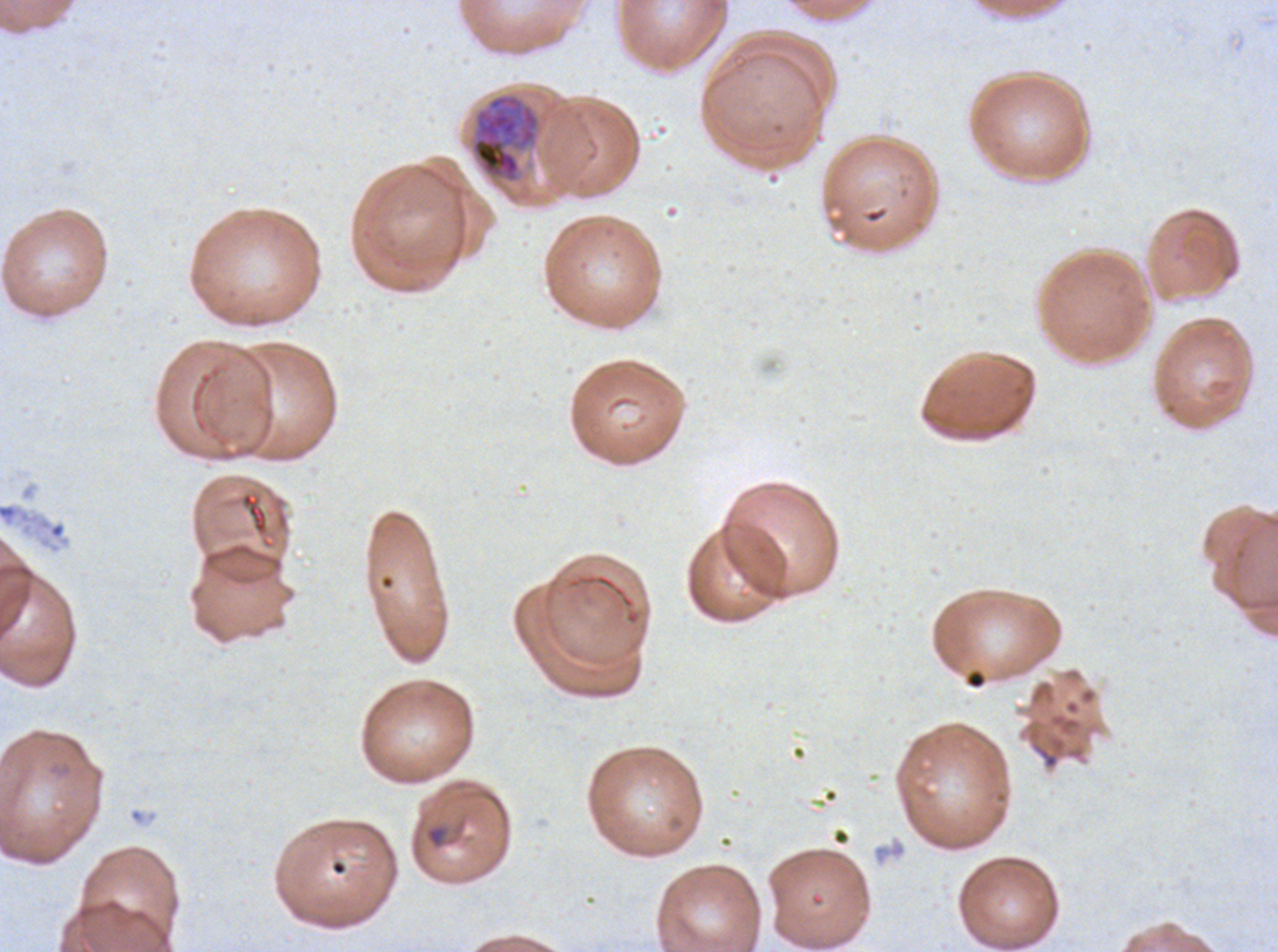

Approximate bounding boxes as (x1, y1, x2, y2) in pixels.
Summary:
  - Early schizont locations: (470, 92, 541, 184)
  - Stain: Giemsa
  - Field of view: one sub-image of a larger composite
  - Image size: 1278×952 pixels
  - Specimen: ex-vivo Plasmodium falciparum culture from a patient in The Gambia, grown for 24 to 48 hours
  - Preparation: thin blood smear